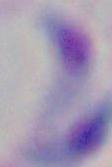
Summary:
  - Identification: Toxoplasma gondii
  - Magnification: 1000x
  - Modality: photomicrograph